Give the position of every Plasmodium parasite visible.
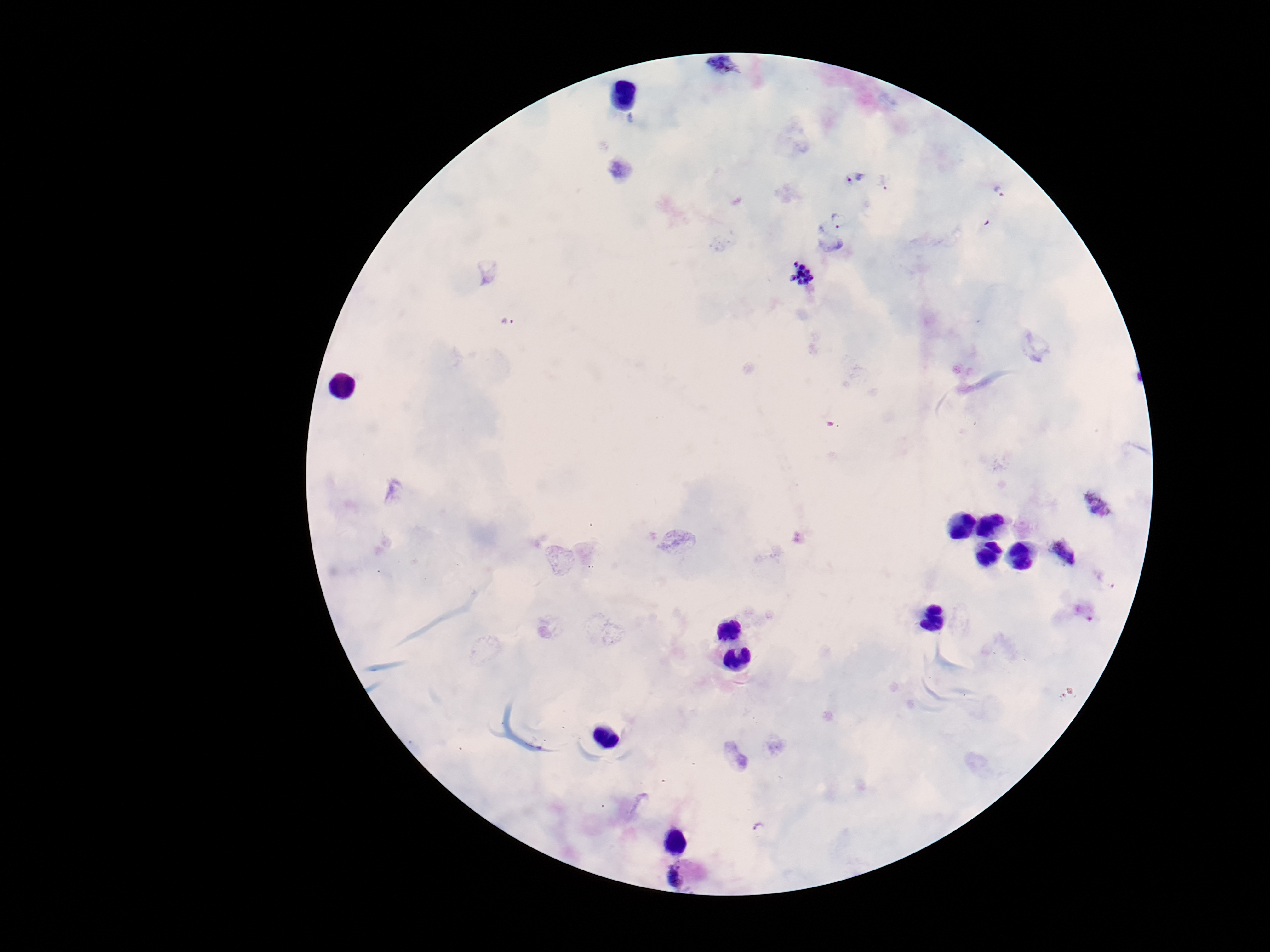

Approximate centers as [x, y] in pixels.
Plasmodium parasites: [723, 66], [853, 177], [883, 182], [998, 191], [833, 233], [803, 276], [508, 323], [1100, 505], [1067, 558], [677, 876].

100x magnification. Smartphone photograph taken through the microscope eyepiece. Patient malaria status: infected. Image is 1270×952 pixels. One field from this slide. Giemsa-stained preparation. Thick peripheral-blood smear.